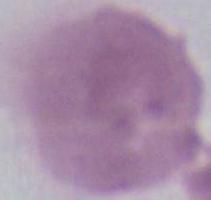 Micrograph. Captured at 1000x magnification. An erythrocyte is shown.